Identify the blood parasite species.
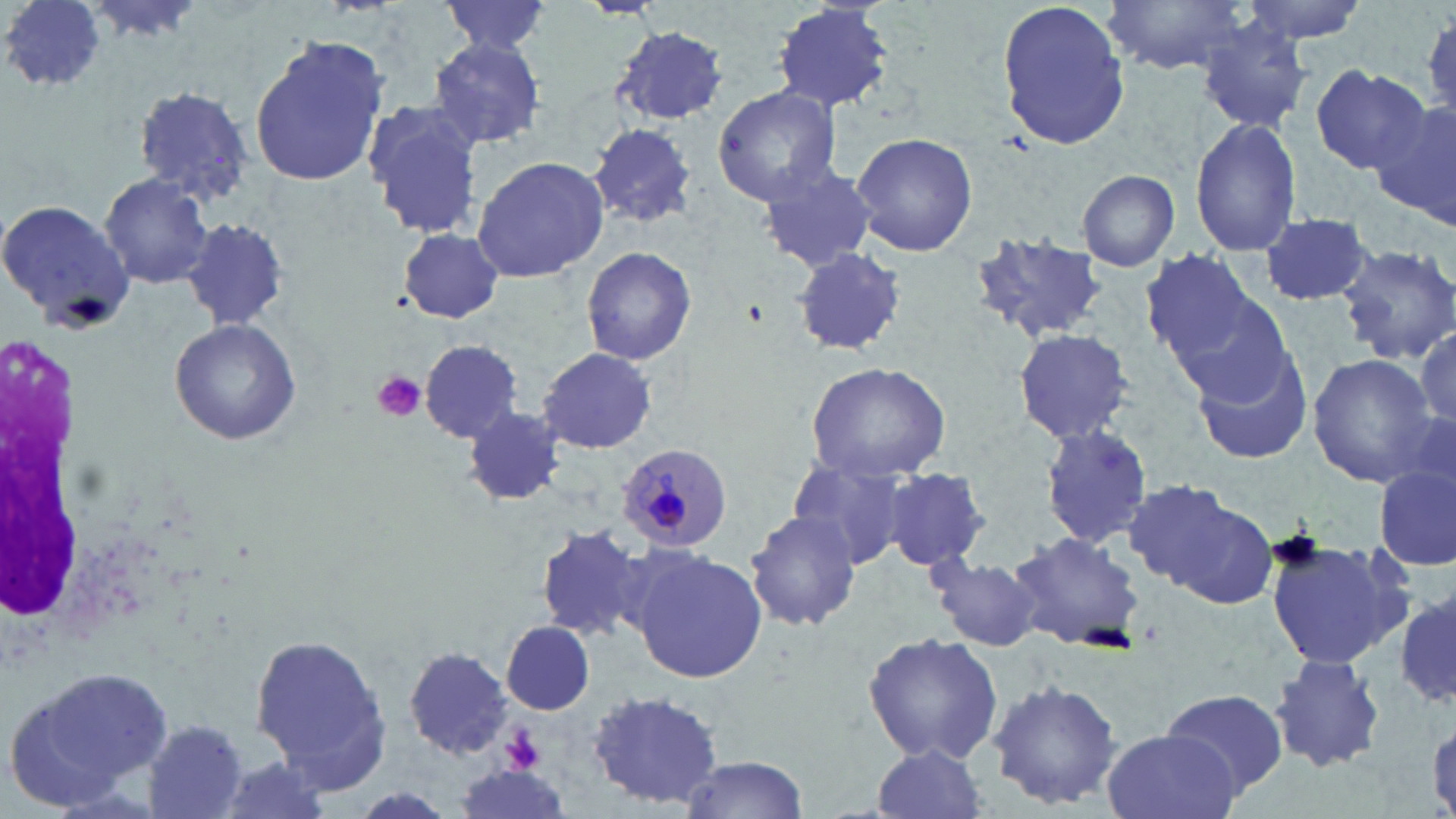

Plasmodium malariae.

Approximate bounding boxes as [x1, y1, x2, y2] in pixels. Plasmodium malariae-infected red blood cell locations: [621, 442, 737, 549]. Uninfected red blood cell locations: [3, 0, 109, 94], [82, 0, 206, 42], [441, 0, 552, 59], [770, 0, 896, 113], [1105, 0, 1253, 75], [1236, 0, 1373, 44], [996, 2, 1133, 150], [1198, 20, 1315, 132], [610, 25, 728, 127], [248, 35, 392, 188], [426, 35, 548, 151], [1309, 65, 1431, 174], [130, 83, 254, 206], [712, 85, 842, 206], [1374, 98, 1456, 226], [360, 100, 486, 236], [1190, 117, 1304, 256], [590, 124, 697, 228], [850, 131, 978, 256], [471, 156, 608, 282], [754, 163, 878, 274], [1078, 169, 1180, 273], [98, 172, 215, 289], [0, 199, 135, 329], [1259, 213, 1378, 307], [183, 218, 288, 331], [397, 228, 508, 323], [969, 232, 1107, 345], [1336, 245, 1456, 363], [581, 246, 698, 365], [790, 246, 909, 357], [1138, 251, 1264, 368], [1163, 282, 1294, 404], [168, 320, 300, 445], [1416, 327, 1455, 427], [1011, 328, 1136, 446], [420, 341, 522, 443], [1189, 344, 1317, 467], [537, 347, 657, 455], [1307, 353, 1438, 487], [806, 359, 952, 482], [463, 407, 567, 507], [1038, 425, 1155, 547], [787, 454, 915, 570], [882, 468, 991, 572], [1375, 469, 1455, 570], [1121, 480, 1273, 605], [745, 509, 862, 632], [534, 523, 650, 644], [1007, 530, 1147, 654], [1263, 533, 1413, 674], [627, 548, 768, 683], [927, 552, 1047, 650], [1397, 591, 1456, 710], [502, 623, 595, 715], [248, 629, 395, 791], [862, 632, 1004, 766], [403, 648, 513, 761], [1270, 653, 1386, 774], [7, 665, 170, 805], [986, 677, 1123, 811], [1159, 688, 1288, 799], [588, 690, 726, 810], [143, 719, 251, 818], [1100, 730, 1242, 819], [866, 745, 991, 819], [207, 754, 337, 819], [677, 756, 811, 817], [454, 767, 573, 817]. Platelet locations: [372, 371, 427, 422], [502, 729, 543, 772]. Image is 1456×819 pixels. Thin blood smear. May-Grünwald-Giemsa-stained preparation. Light microscopy. Captured at 1000x magnification. One field of a larger specimen.